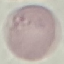

Summary:
  - Malaria status: uninfected
  - Stain: Giemsa
  - Capture: smartphone through the microscope eyepiece
  - Preparation: thin smear
  - Image type: cell patch, automatically extracted from a larger field of view and resized to 64 × 64 pixels